Give the position of every leukocyte visible.
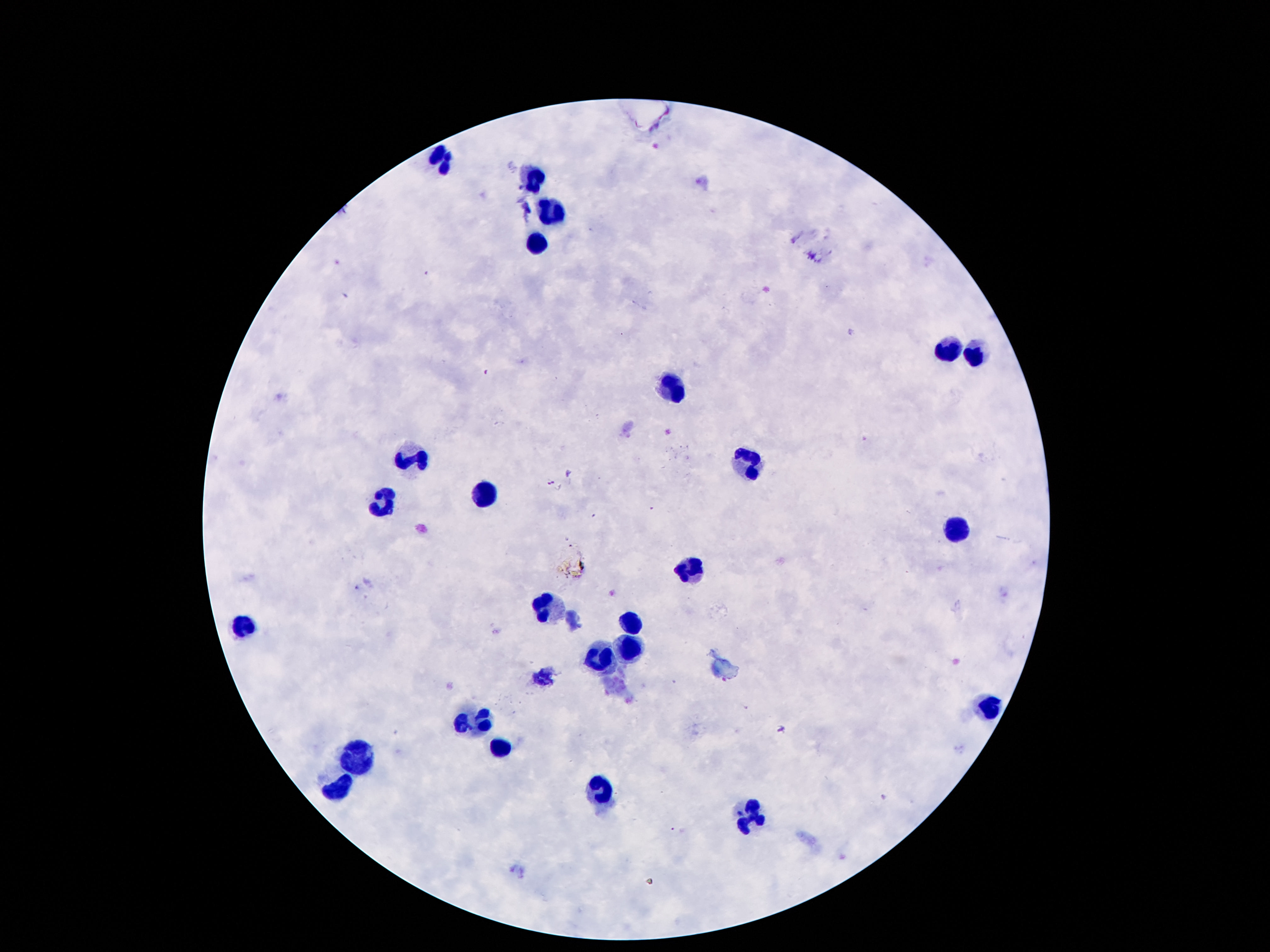

Approximate centers as (x, y) in pixels.
Leukocytes: (439, 156), (535, 178), (553, 213), (535, 241), (948, 351), (976, 360), (672, 388), (411, 458), (752, 464), (486, 495), (383, 505), (962, 530), (696, 568), (550, 608), (631, 624), (246, 626), (631, 651), (603, 659), (994, 708), (476, 725), (503, 751), (356, 759), (608, 787), (339, 788), (750, 820).

Giemsa stain. 100x magnification. One field from this slide. Image is 1270×952 pixels. Thick blood film. Photographed through the microscope eyepiece with a smartphone camera. Patient malaria status: not infected.